Report the malaria status of this cell.
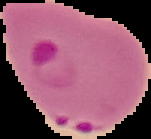

Parasitized.

image type = segmented cell region with the area outside set to black
preparation = thin blood film
image size = 151×139 pixels